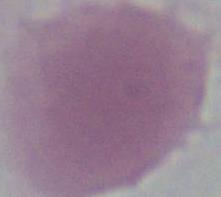

Captured at 1000x magnification. Photomicrograph. An erythrocyte is shown.